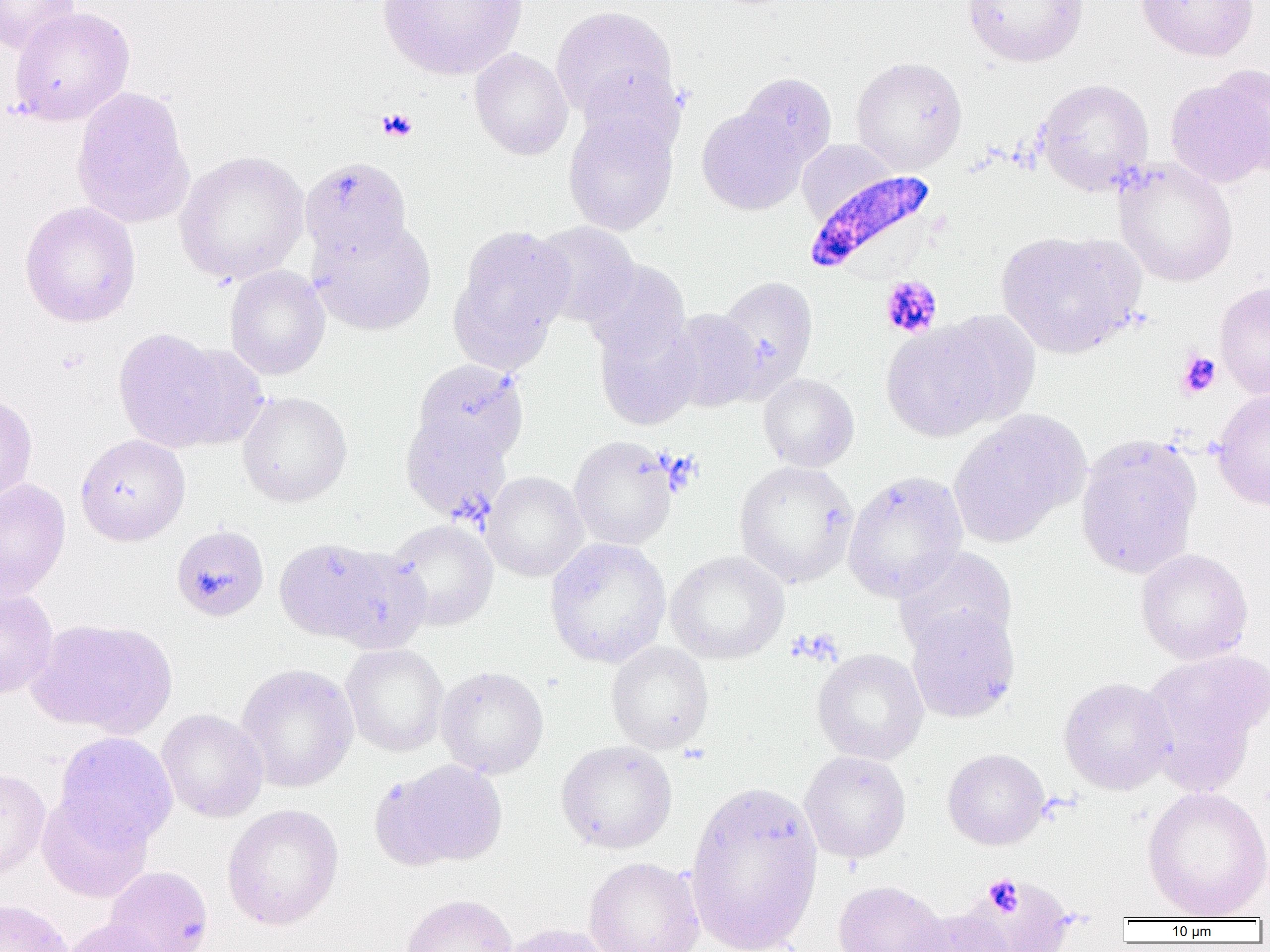

Approximate bounding boxes as (x1,y1)-(x2,y2) corner pairs in pixels. Plasmodium falciparum-infected red blood cell locations: (802,169)-(939,281). Uninfected red blood cell locations: (0,0)-(80,55), (377,0)-(528,81), (962,0)-(1088,66), (1135,0)-(1259,61), (551,6)-(677,119), (10,7)-(135,126), (469,47)-(573,161), (850,56)-(968,174), (577,66)-(685,161), (737,72)-(837,170), (1165,72)-(1269,189), (1035,79)-(1154,196), (71,86)-(194,228), (696,106)-(808,214), (563,110)-(678,234), (796,139)-(900,223), (174,150)-(310,285), (300,157)-(412,263), (1114,158)-(1238,287), (19,201)-(141,328), (309,218)-(436,335), (531,221)-(640,326), (449,225)-(575,369), (995,229)-(1144,358), (581,257)-(690,363), (224,265)-(330,380), (714,276)-(819,397), (1214,281)-(1270,399), (666,308)-(764,412), (929,309)-(1041,428), (593,313)-(701,430), (880,321)-(1007,442), (113,328)-(242,453), (412,359)-(529,464), (757,373)-(859,472), (1211,388)-(1270,511), (237,391)-(352,506), (0,392)-(38,509), (947,410)-(1087,548), (400,413)-(511,524), (1075,433)-(1202,579), (75,434)-(190,545), (568,436)-(678,550), (734,460)-(859,588), (842,470)-(968,603), (481,471)-(588,581), (0,479)-(71,599), (385,519)-(499,631), (171,530)-(268,619), (273,536)-(397,645), (544,537)-(672,668), (326,545)-(429,654), (894,547)-(1017,656), (1135,548)-(1254,664), (665,550)-(789,664), (0,586)-(58,699), (905,605)-(1019,723), (26,618)-(176,738), (606,641)-(714,754), (340,644)-(449,756), (812,648)-(929,765), (1140,650)-(1268,791), (235,663)-(359,792), (436,665)-(549,778), (1058,677)-(1176,795), (156,708)-(269,822), (54,731)-(179,849), (555,740)-(677,854), (943,748)-(1050,850), (799,750)-(911,864), (374,758)-(508,870), (0,768)-(51,881), (685,780)-(823,952), (1141,786)-(1270,920), (37,792)-(154,903), (222,803)-(344,930), (584,857)-(705,952), (103,865)-(213,952), (975,876)-(1074,952), (832,880)-(951,952), (400,894)-(519,952), (0,898)-(73,952), (903,906)-(1015,951), (63,919)-(167,952), (500,922)-(616,952). Platelet locations: (376,107)-(418,142), (880,275)-(942,338), (1175,350)-(1222,398), (791,629)-(842,666), (982,874)-(1024,917). Slide-level diagnosis: Plasmodium falciparum. Thin blood smear. 1000x magnification. One field of a larger specimen. Optical microscopy. Image is 1270×952 pixels.